Assess this cell for malaria.
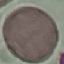

It is uninfected.

capture = smartphone camera at the microscope eyepiece
preparation = thin blood film
image type = cell patch, automatically extracted from a larger field of view and resized to 64 × 64 pixels
stain = Giemsa